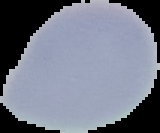 Image is 160×133 pixels. Malaria status: uninfected. Segmented cell region on a black background. From a thin blood film.